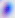

magnification: 400x
identification: Toxoplasma gondii
modality: photomicrograph